Classify this cell by malaria status.
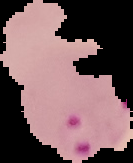

Parasitized.

From a thin blood smear. Segmented cell region on a black background. Image is 133×163 pixels.